Locate and identify every blood parasite.
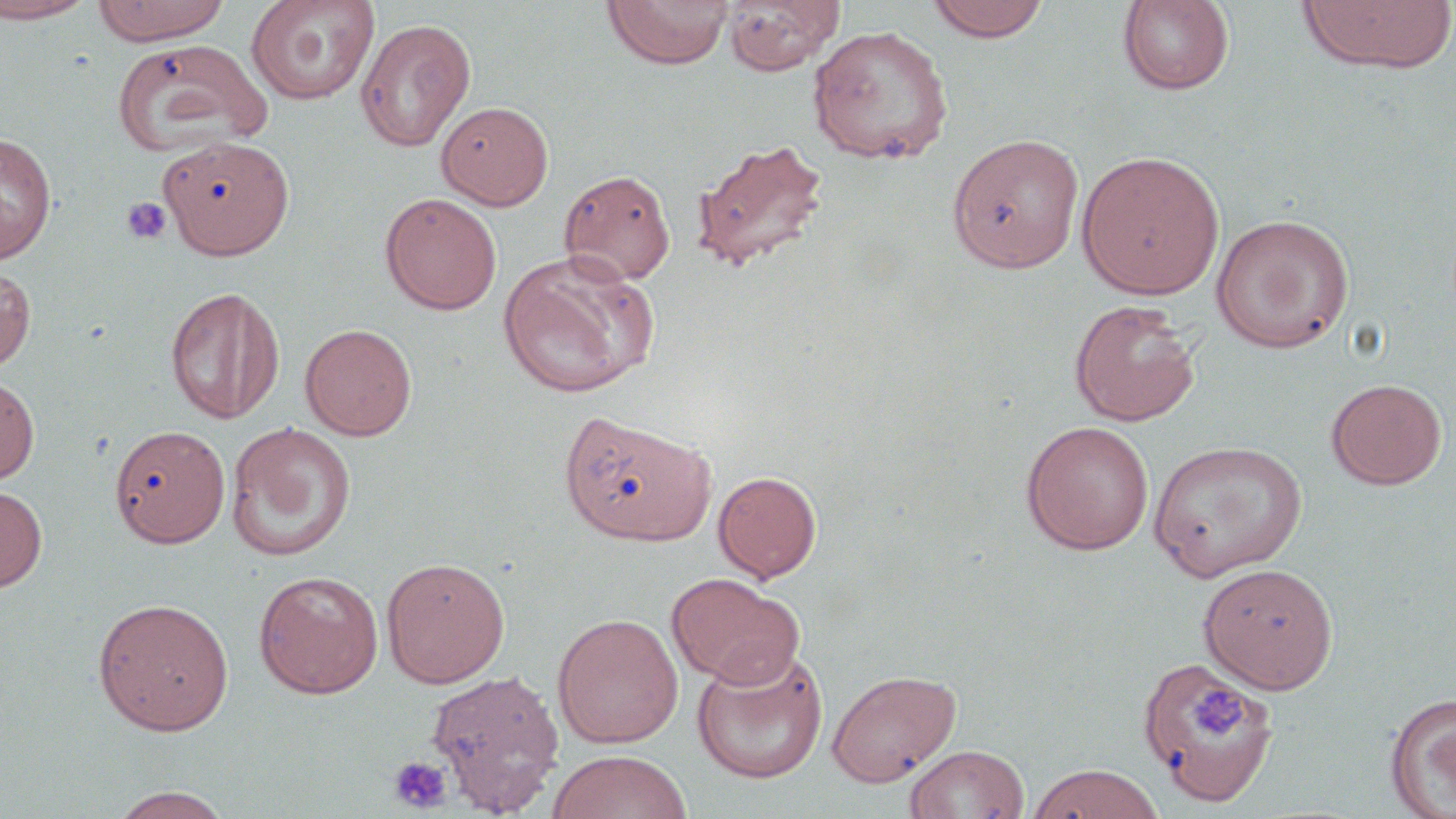
No blood parasites observed.

Approximate bounding boxes as [x1, y1, x2, y2] in pixels. Platelet locations: [120, 195, 173, 246], [1188, 683, 1251, 742], [388, 756, 453, 813]. Uninfected red blood cell locations: [0, 0, 97, 23], [92, 0, 231, 45], [246, 0, 379, 105], [602, 0, 733, 70], [926, 0, 1051, 43], [1117, 0, 1236, 95], [1296, 0, 1456, 76], [722, 1, 844, 75], [355, 18, 476, 151], [807, 25, 954, 166], [112, 38, 272, 160], [436, 100, 553, 210], [410, 120, 563, 296], [0, 131, 57, 262], [946, 133, 1085, 273], [160, 136, 294, 260], [692, 138, 830, 274], [1076, 150, 1225, 299], [558, 169, 676, 286], [379, 192, 502, 315], [1210, 212, 1356, 353], [497, 251, 658, 399], [0, 262, 36, 374], [164, 284, 285, 425], [1069, 298, 1201, 426], [300, 323, 418, 441], [0, 371, 39, 487], [1325, 378, 1447, 490], [557, 408, 717, 546], [1020, 420, 1155, 555], [226, 422, 357, 562], [108, 423, 231, 548], [1148, 440, 1308, 582], [713, 470, 821, 583], [0, 483, 48, 592], [381, 556, 510, 688], [1198, 562, 1339, 693], [253, 569, 384, 698], [665, 572, 805, 689], [92, 597, 234, 735], [552, 613, 683, 747], [692, 646, 828, 785], [1137, 654, 1280, 808], [426, 668, 565, 814], [826, 668, 962, 787], [1384, 691, 1456, 818], [905, 744, 1030, 819], [546, 750, 692, 819], [1029, 763, 1165, 819], [106, 786, 235, 819]. Slide-level diagnosis: no evidence of blood parasites. Optical microscopy. Thin blood film. 1000x magnification. Single field of view. May-Grünwald-Giemsa stain. Image is 1456×819 pixels.